Describe the morphology of the erythrocytes.
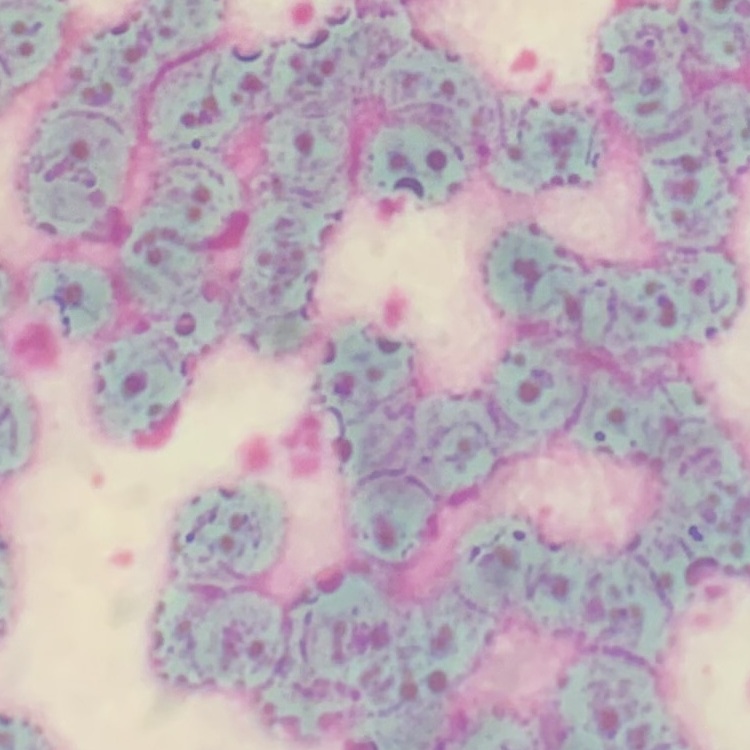
They show rouleaux formation.

image type = square crop of a larger photomicrograph
stain = Field's or Giemsa
preparation = thin peripheral smear